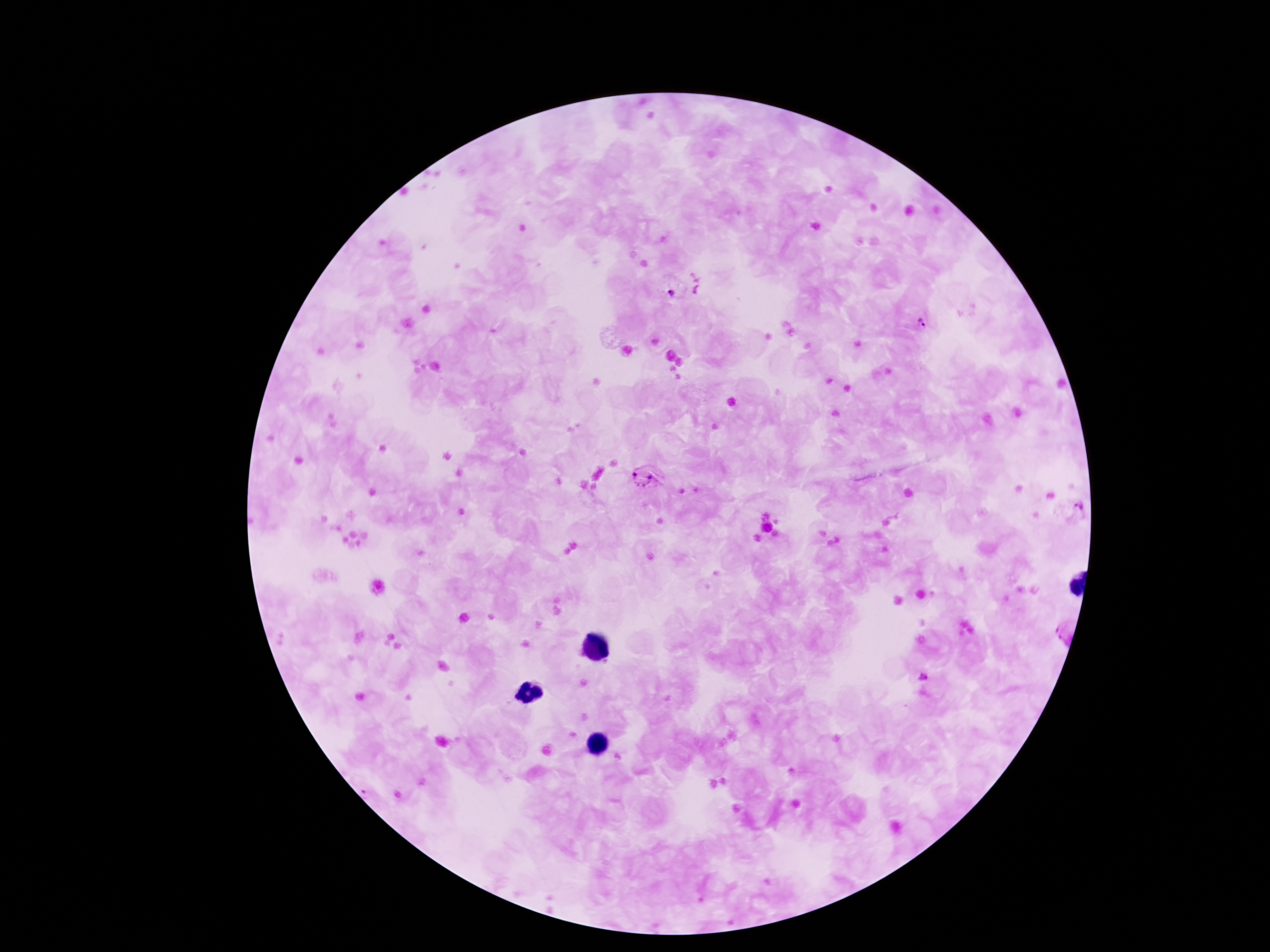

field of view = single
Plasmodium parasite locations = approximate object centers, in pixels from the top-left corner: (x=922, y=324), (x=645, y=478), (x=1078, y=513), (x=1055, y=631)
preparation = thick blood smear
capture = smartphone camera through the microscope eyepiece
stain = Giemsa
magnification = 100x
image size = 1270×952 pixels
patient malaria status = positive